Describe the morphology of the red blood cells.
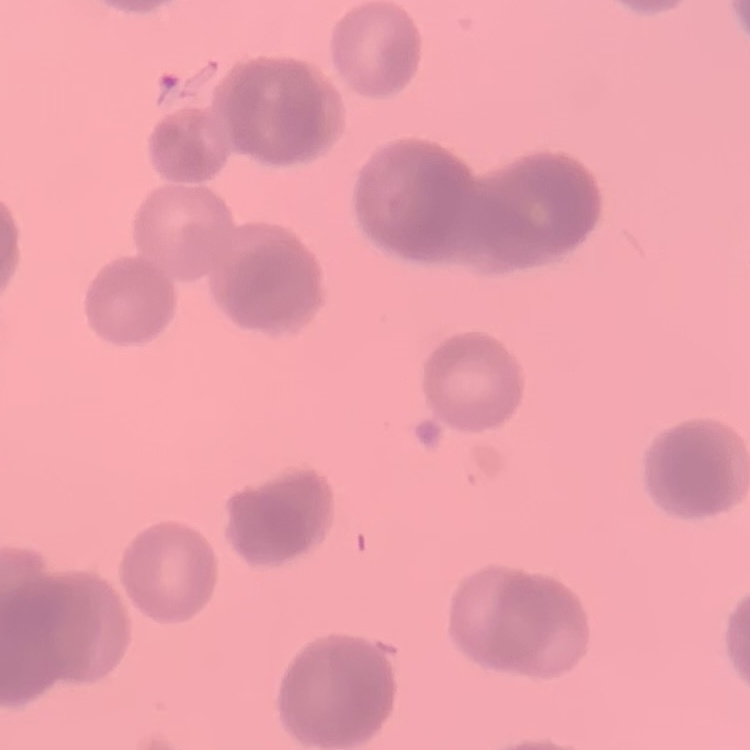

Rouleaux formation.

image type = square crop of a larger photomicrograph
preparation = thin peripheral smear
stain = Field's or Giemsa